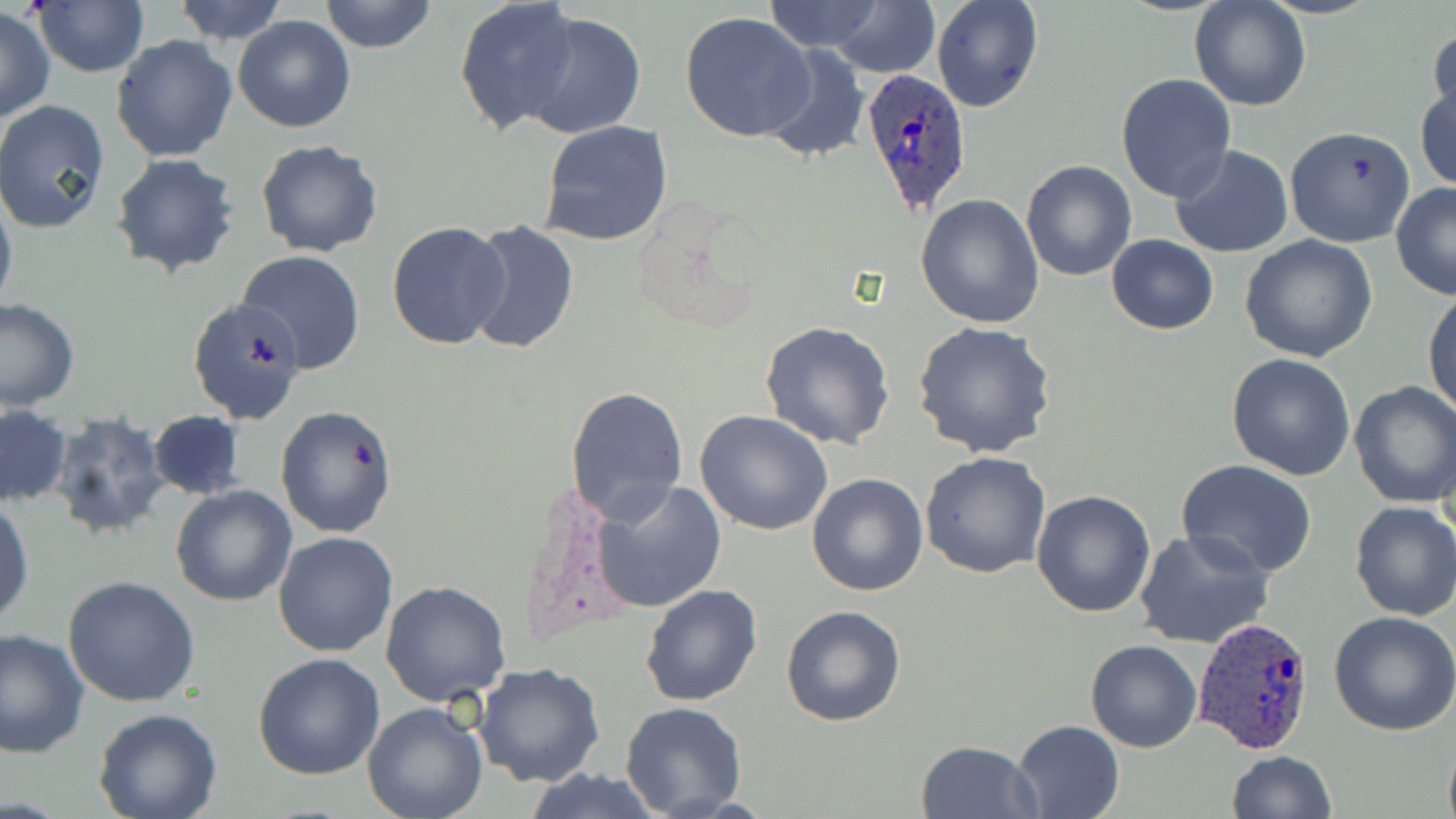 Approximate bounding boxes as (x1,y1)-(x2,y2) corner pairs in pixels. Uninfected red blood cell locations: (31,0)-(149,77), (170,0)-(290,44), (318,0)-(438,53), (454,0)-(584,136), (759,0)-(895,55), (932,0)-(1043,113), (1188,0)-(1311,113), (825,3)-(939,78), (1,6)-(54,123), (679,10)-(817,143), (515,11)-(647,140), (233,15)-(356,133), (1427,24)-(1456,128), (111,35)-(238,161), (760,43)-(872,163), (1115,73)-(1236,203), (1416,76)-(1456,195), (0,100)-(111,234), (537,120)-(673,247), (1285,125)-(1416,247), (255,140)-(384,258), (1171,144)-(1293,257), (111,153)-(241,276), (1021,159)-(1138,281), (0,179)-(17,320), (1390,182)-(1456,299), (915,193)-(1044,329), (463,219)-(579,358), (387,222)-(512,350), (1107,234)-(1218,335), (1240,234)-(1377,362), (237,250)-(364,373), (1424,285)-(1456,420), (188,296)-(310,425), (0,297)-(80,412), (758,319)-(896,450), (912,320)-(1057,458), (1227,353)-(1356,479), (1349,381)-(1456,507), (566,386)-(689,521), (275,404)-(398,538), (1,406)-(72,508), (695,410)-(835,536), (146,411)-(248,499), (46,412)-(172,543), (920,451)-(1052,578), (1175,460)-(1320,581), (807,472)-(928,595), (588,479)-(727,614), (170,485)-(296,606), (1030,489)-(1156,618), (0,497)-(34,629), (1350,500)-(1456,621), (1133,528)-(1274,649), (274,532)-(398,657), (62,575)-(200,708), (380,579)-(510,705), (640,583)-(763,706), (781,605)-(907,728), (1327,610)-(1456,737), (0,628)-(90,757), (1084,640)-(1201,753), (252,652)-(385,778), (474,663)-(605,787), (365,684)-(600,806), (362,701)-(489,819), (620,702)-(748,818), (93,710)-(221,819), (1011,719)-(1124,819), (915,739)-(1043,818), (1225,750)-(1338,819), (524,767)-(665,819). Plasmodium ovale-infected red blood cell locations: (861,67)-(974,216), (1191,616)-(1320,757). Slide-level diagnosis: Plasmodium ovale. Image is 1456×819 pixels. Thin blood film. Optical microscopy. Single field of view. May-Grünwald-Giemsa stain. 1000x magnification.